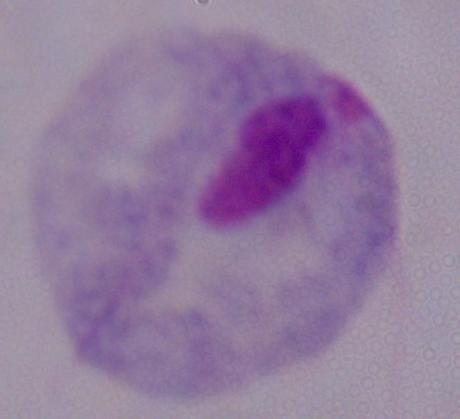
identification = trichomonad
magnification = 1000x
modality = photomicrograph